State the blood parasite species.
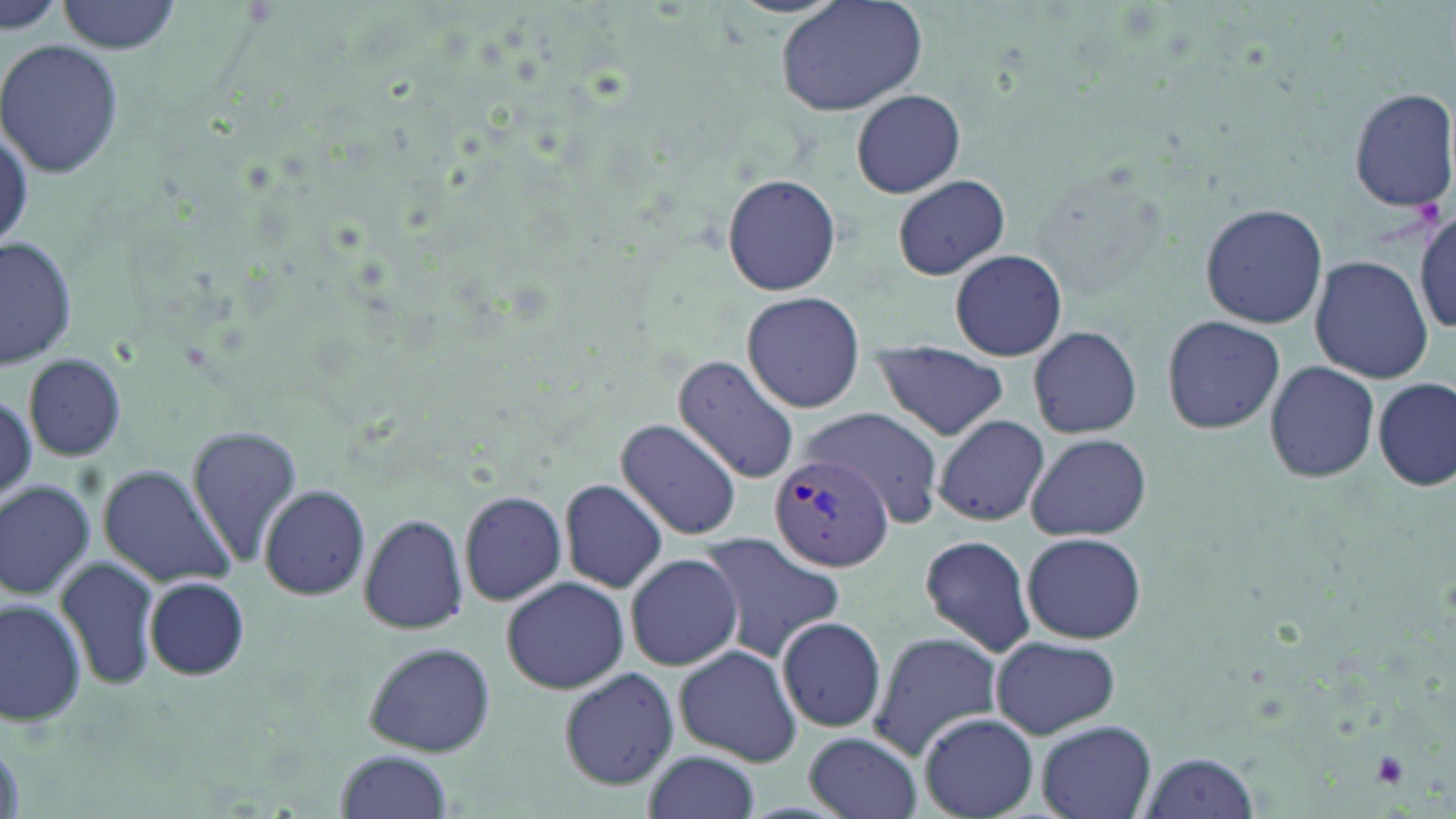
Plasmodium vivax.

Approximate bounding boxes as (x1, y1, x2, y2) in pixels. Uninfected red blood cell locations: (0, 0, 62, 36), (58, 0, 183, 53), (774, 0, 926, 117), (0, 40, 125, 180), (1348, 87, 1455, 211), (852, 89, 963, 198), (720, 173, 844, 296), (892, 175, 1010, 280), (1201, 203, 1328, 328), (1412, 210, 1456, 338), (0, 236, 78, 369), (949, 249, 1067, 361), (1310, 255, 1432, 384), (741, 291, 866, 413), (1163, 314, 1285, 434), (1025, 326, 1142, 440), (870, 340, 1009, 441), (23, 354, 128, 461), (672, 356, 799, 485), (1262, 359, 1380, 484), (1373, 377, 1454, 492), (804, 406, 946, 526), (933, 414, 1049, 528), (616, 419, 742, 540), (186, 424, 302, 565), (1025, 432, 1151, 543), (99, 465, 236, 585), (560, 478, 667, 593), (1, 480, 97, 601), (258, 484, 371, 602), (458, 490, 569, 608), (357, 512, 468, 636), (1021, 531, 1146, 643), (695, 533, 848, 662), (918, 533, 1037, 657), (625, 553, 742, 671), (55, 554, 161, 693), (145, 576, 250, 681), (501, 577, 628, 694), (0, 596, 86, 725), (774, 617, 888, 732), (867, 631, 1000, 760), (991, 635, 1120, 739), (361, 641, 497, 757), (674, 644, 803, 766), (559, 666, 679, 790), (920, 714, 1038, 817), (1036, 720, 1156, 819), (805, 732, 922, 819), (641, 748, 761, 819), (334, 749, 455, 819), (1137, 751, 1260, 819). Platelet locations: (1369, 750, 1410, 787). Plasmodium vivax-infected red blood cell locations: (770, 448, 893, 572). One field of a larger specimen. 1000x magnification. Thin blood smear. Light microscopy. May-Grünwald-Giemsa stain. Image is 1456×819 pixels.